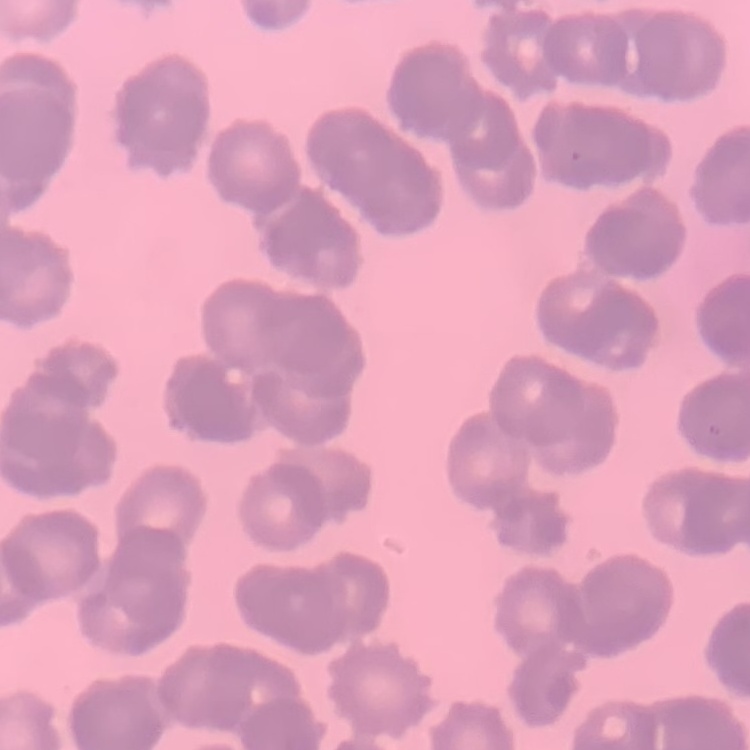
The red blood cells show rouleaux formation. Thin blood film. Square crop of a larger photomicrograph. Field's or Giemsa stain.